Identify the parasite.
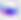
This is Toxoplasma gondii.

Summary:
  - Magnification: 400x
  - Modality: micrograph